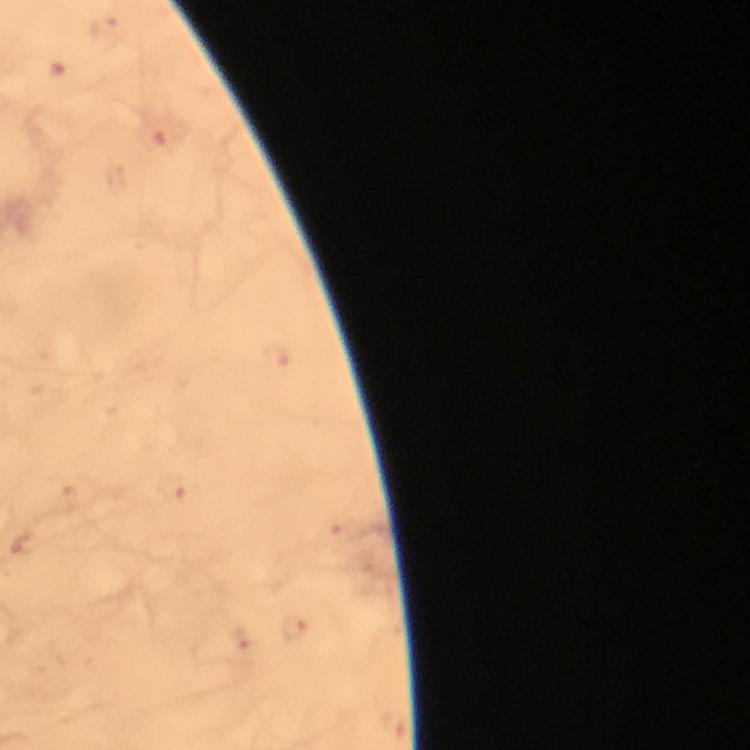

Approximate object centers, in pixels from the top-left corner.
Summary:
  - Plasmodium parasite locations: (x=109, y=27), (x=174, y=488), (x=298, y=630)
  - Context: from a diagnostic examination for malaria
  - Image size: 750×750 pixels
  - Stain: Giemsa
  - Immersion oil: applied
  - Cropped from: a single field of view
  - Magnification: 100x
  - Capture: smartphone photograph through a microscope
  - Preparation: thick smear